Comment on the morphology of the erythrocytes.
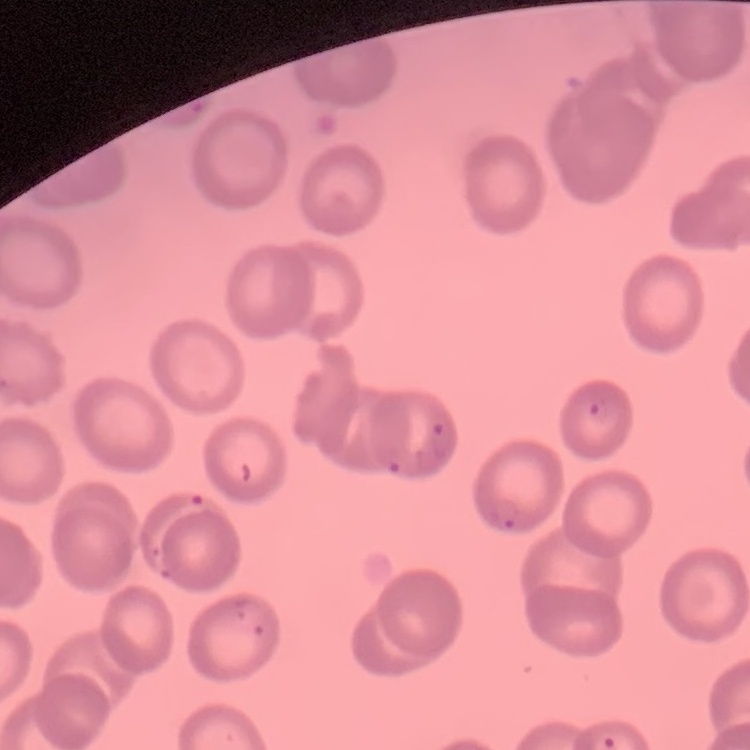
No rouleaux formation.

Square crop of a larger photomicrograph. Field's or Giemsa stain. Thin blood smear.